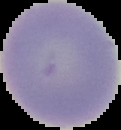
Summary:
  - Image size: 121×130 pixels
  - Preparation: thin blood smear
  - Image type: cell region segmented out of the field of view; surrounding area masked to black
  - Malaria status: uninfected